Outline each blood parasite and name the species.
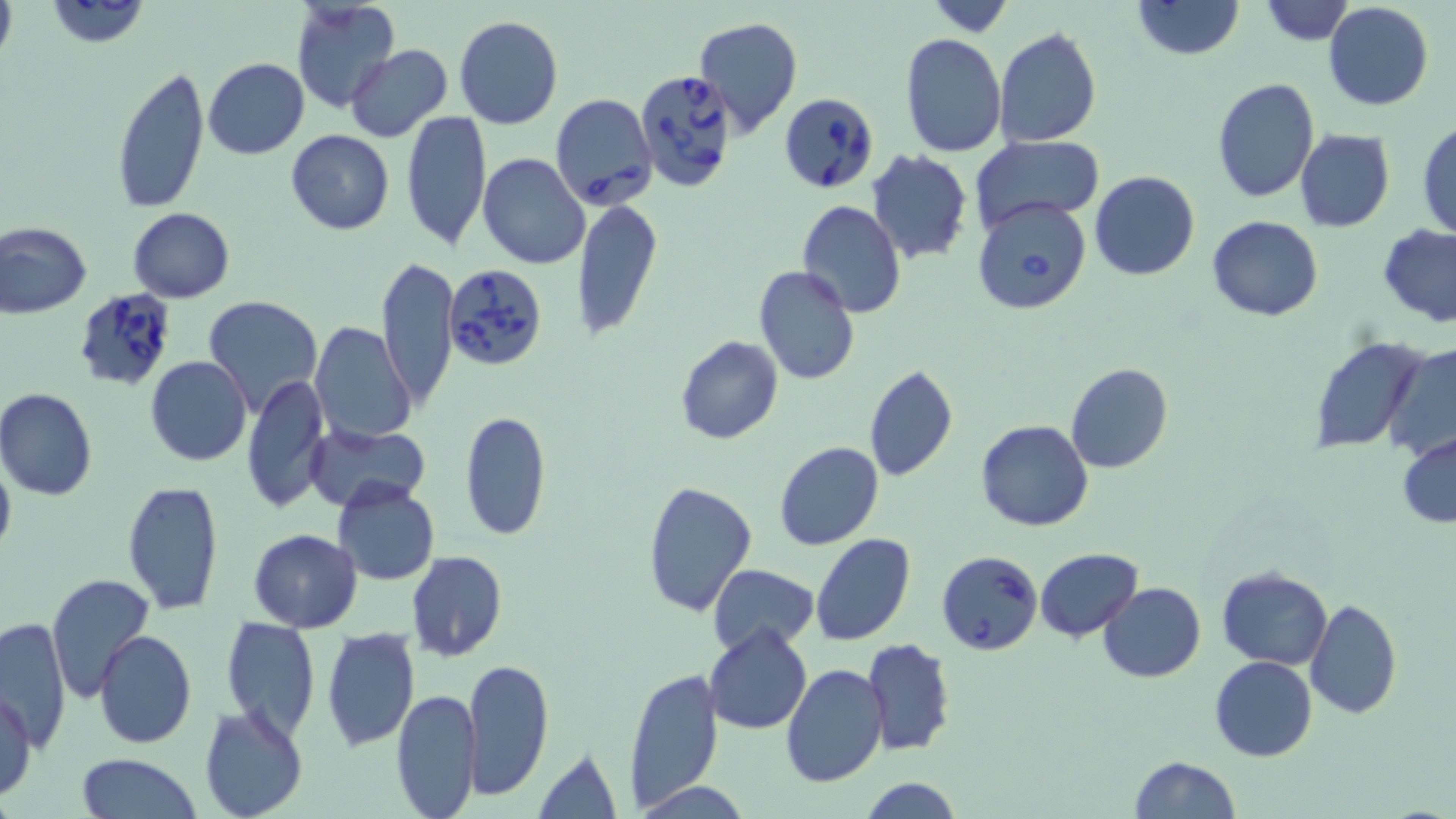
Approximate bounding boxes as named x1/y1/x2/y2 corners in pixels.
Babesia divergens-infected red blood cells: (x1=634, y1=69, x2=740, y2=194), (x1=781, y1=90, x2=883, y2=194), (x1=550, y1=93, x2=657, y2=211), (x1=973, y1=197, x2=1092, y2=313), (x1=446, y1=264, x2=549, y2=375), (x1=71, y1=288, x2=179, y2=393), (x1=936, y1=550, x2=1043, y2=656).
No Plasmodium falciparum, Plasmodium ovale, Plasmodium malariae, Plasmodium vivax, or Trypanosoma brucei observed.

slide-level diagnosis = Babesia divergens
image size = 1456×819 pixels
modality = optical microscopy
magnification = 1000x
stain = May-Grünwald-Giemsa
field of view = single
preparation = thin blood smear
uninfected red blood cell locations = approximate bounding boxes as named x1/y1/x2/y2 corners in pixels: (x1=0, y1=0, x2=16, y2=67), (x1=44, y1=0, x2=150, y2=48), (x1=289, y1=0, x2=400, y2=114), (x1=1133, y1=0, x2=1243, y2=60), (x1=924, y1=2, x2=1017, y2=34), (x1=1259, y1=2, x2=1355, y2=46), (x1=1323, y1=3, x2=1434, y2=112), (x1=455, y1=17, x2=563, y2=129), (x1=694, y1=17, x2=805, y2=139), (x1=994, y1=27, x2=1102, y2=148), (x1=901, y1=34, x2=1006, y2=156), (x1=346, y1=45, x2=453, y2=143), (x1=202, y1=57, x2=310, y2=159), (x1=111, y1=65, x2=211, y2=213), (x1=1211, y1=79, x2=1321, y2=204), (x1=403, y1=109, x2=491, y2=251), (x1=428, y1=124, x2=570, y2=259), (x1=1417, y1=125, x2=1456, y2=241), (x1=285, y1=129, x2=395, y2=234), (x1=1295, y1=129, x2=1395, y2=232), (x1=971, y1=136, x2=1102, y2=236), (x1=865, y1=150, x2=973, y2=264), (x1=478, y1=153, x2=591, y2=271), (x1=1088, y1=172, x2=1200, y2=280), (x1=572, y1=199, x2=661, y2=339), (x1=796, y1=201, x2=906, y2=317), (x1=127, y1=207, x2=234, y2=302), (x1=1209, y1=216, x2=1323, y2=322), (x1=0, y1=221, x2=92, y2=317), (x1=1378, y1=223, x2=1456, y2=327), (x1=375, y1=255, x2=460, y2=411), (x1=754, y1=266, x2=861, y2=386), (x1=202, y1=296, x2=323, y2=418), (x1=310, y1=322, x2=415, y2=444), (x1=673, y1=335, x2=784, y2=445), (x1=1309, y1=338, x2=1429, y2=453), (x1=1384, y1=344, x2=1456, y2=462), (x1=146, y1=356, x2=253, y2=466), (x1=1065, y1=363, x2=1173, y2=473), (x1=863, y1=364, x2=958, y2=483), (x1=242, y1=373, x2=331, y2=514), (x1=0, y1=389, x2=98, y2=501), (x1=460, y1=410, x2=551, y2=542), (x1=976, y1=419, x2=1093, y2=531), (x1=305, y1=422, x2=431, y2=511), (x1=1397, y1=434, x2=1456, y2=527), (x1=774, y1=442, x2=885, y2=551), (x1=0, y1=455, x2=16, y2=559), (x1=642, y1=479, x2=755, y2=617), (x1=121, y1=480, x2=225, y2=616), (x1=332, y1=481, x2=440, y2=586), (x1=248, y1=528, x2=362, y2=631), (x1=812, y1=533, x2=915, y2=647), (x1=1035, y1=549, x2=1142, y2=641), (x1=406, y1=551, x2=509, y2=662), (x1=708, y1=563, x2=818, y2=654), (x1=1216, y1=567, x2=1333, y2=670), (x1=43, y1=574, x2=150, y2=699), (x1=1098, y1=581, x2=1205, y2=683), (x1=1306, y1=598, x2=1402, y2=719), (x1=2, y1=616, x2=72, y2=747), (x1=219, y1=617, x2=322, y2=740), (x1=704, y1=625, x2=813, y2=734), (x1=320, y1=626, x2=419, y2=752), (x1=95, y1=629, x2=197, y2=747), (x1=861, y1=637, x2=956, y2=758), (x1=1209, y1=655, x2=1317, y2=761), (x1=463, y1=657, x2=553, y2=800), (x1=779, y1=663, x2=888, y2=786), (x1=624, y1=667, x2=725, y2=809), (x1=0, y1=688, x2=38, y2=803), (x1=391, y1=688, x2=482, y2=817), (x1=198, y1=703, x2=309, y2=819), (x1=534, y1=747, x2=624, y2=817), (x1=76, y1=754, x2=204, y2=818), (x1=1129, y1=756, x2=1239, y2=818), (x1=859, y1=778, x2=964, y2=817)